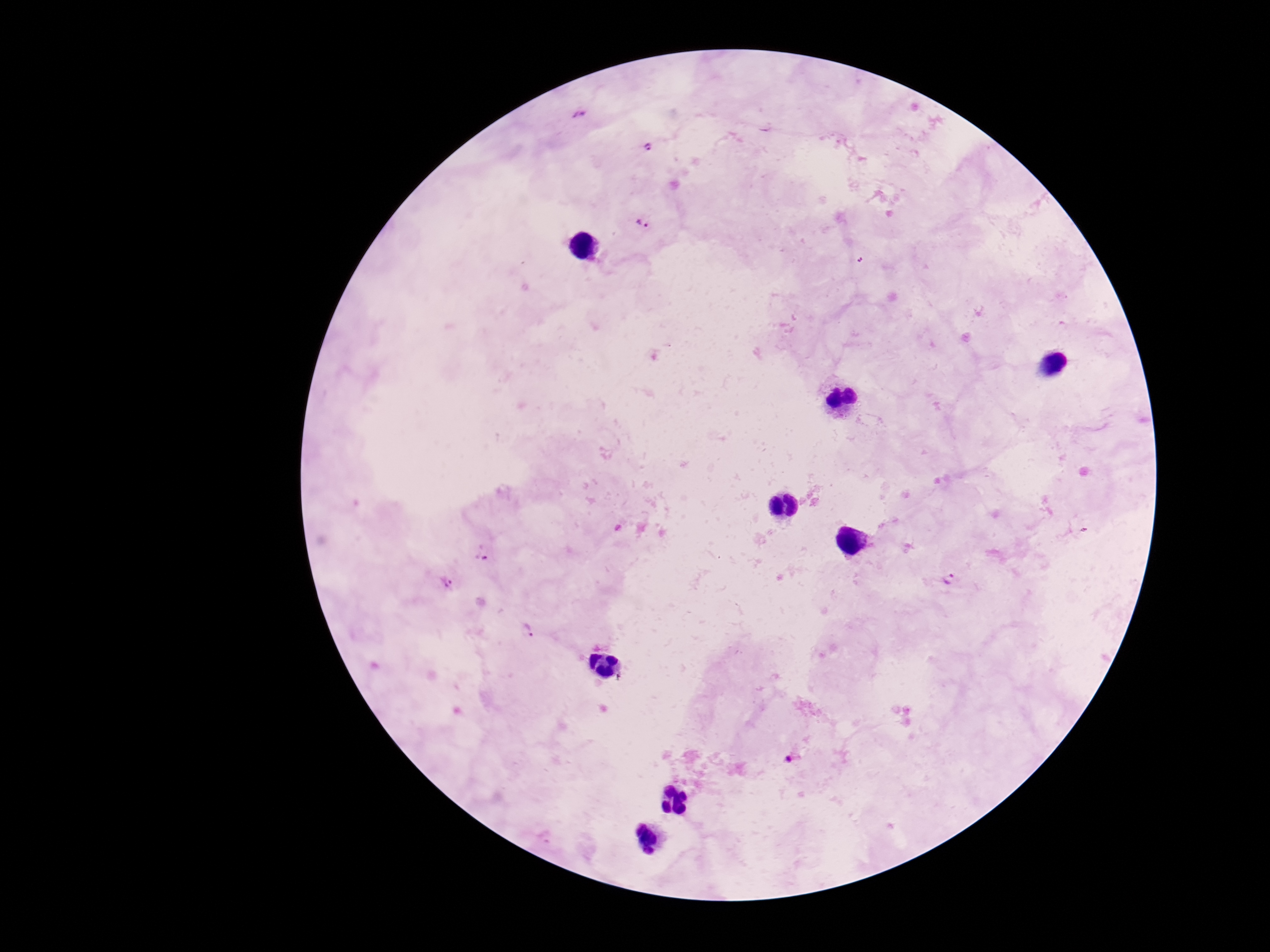
{
  "magnification": "100x",
  "preparation": "thick blood film",
  "capture": "smartphone camera through the microscope eyepiece",
  "patient_malaria_status": "infected",
  "stain": "Giemsa",
  "image_size": "1270×952 pixels",
  "plasmodium_parasite_locations": "approximate centers as (x, y) in pixels: (579, 115), (647, 145), (642, 222), (483, 554), (949, 580), (444, 582), (526, 631), (791, 760)",
  "field_of_view": "one from this slide"
}